Assess this cell for malaria.
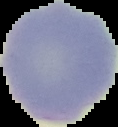
It is uninfected.

{
  "image_size": "118×127 pixels",
  "image_type": "segmented cell region on a black background",
  "preparation": "thin blood film"
}